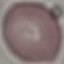

result = negative for malaria parasites
image type = automatically extracted cell patch, resized to 64 × 64 pixels
stain = Giemsa
preparation = thin blood film
capture = smartphone camera at the microscope eyepiece